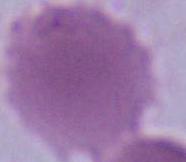
{
  "identification": "red blood cell",
  "modality": "micrograph",
  "magnification": "1000x"
}